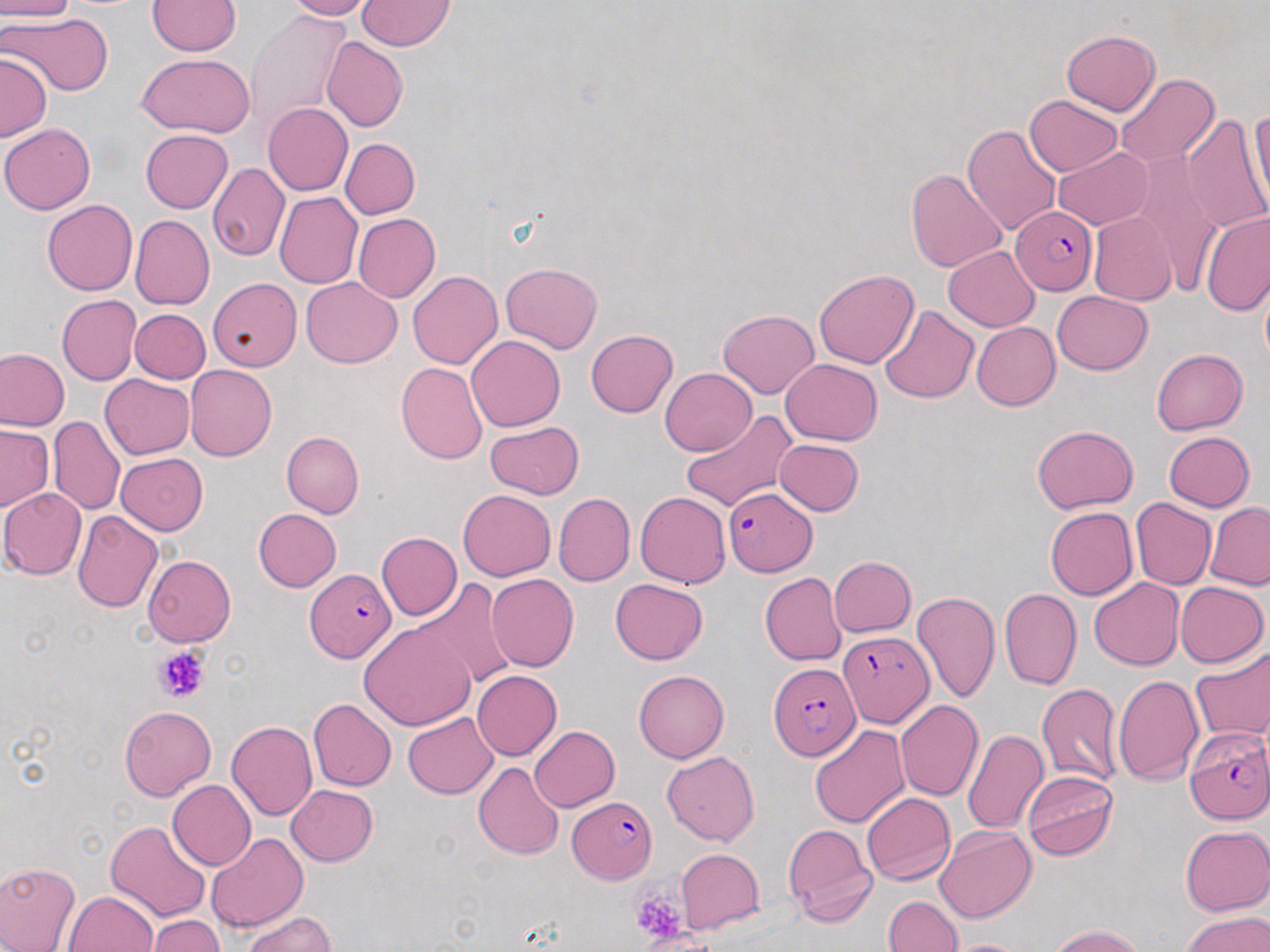

slide-level diagnosis = Plasmodium falciparum
modality = optical microscopy
preparation = thin blood smear
image size = 1270×952 pixels
magnification = 1000x
field of view = single
Plasmodium falciparum-infected red blood cell locations = approximate bounding boxes as (x1, y1, x2, y2) in pixels: (1014, 205, 1097, 292), (723, 486, 816, 576), (305, 567, 397, 663), (837, 632, 930, 728), (768, 661, 859, 761), (1185, 727, 1270, 826), (566, 796, 657, 883)
uninfected red blood cell locations = approximate bounding boxes as (x1, y1, x2, y2) in pixels: (0, 0, 76, 21), (281, 0, 373, 21), (356, 0, 454, 50), (147, 1, 242, 56), (246, 10, 353, 131), (3, 13, 112, 96), (1060, 30, 1160, 116), (322, 36, 408, 132), (0, 52, 51, 141), (137, 52, 254, 137), (1114, 74, 1221, 168), (1025, 94, 1122, 177), (263, 102, 352, 196), (1245, 109, 1270, 221), (1180, 114, 1268, 235), (0, 123, 95, 214), (962, 123, 1061, 238), (140, 129, 234, 213), (340, 139, 419, 219), (1054, 146, 1152, 229), (1130, 155, 1225, 295), (207, 162, 290, 262), (904, 167, 1008, 275), (274, 192, 362, 289), (42, 200, 137, 295), (1088, 211, 1176, 306), (1201, 211, 1270, 317), (353, 213, 440, 303), (129, 215, 214, 310), (943, 246, 1041, 332), (500, 262, 602, 354), (813, 269, 919, 369), (407, 271, 503, 370), (300, 277, 403, 368), (208, 278, 302, 372), (1052, 290, 1151, 374), (56, 295, 142, 385), (878, 305, 980, 404), (718, 308, 819, 399), (130, 309, 210, 383), (971, 322, 1060, 410), (585, 330, 677, 418), (467, 335, 565, 432), (0, 348, 70, 432), (1152, 349, 1248, 435), (782, 358, 882, 445), (396, 362, 488, 465), (185, 365, 277, 462), (660, 368, 757, 456), (100, 373, 194, 460), (680, 409, 796, 512), (48, 416, 125, 515), (485, 421, 584, 499), (0, 424, 53, 511), (1032, 425, 1138, 512), (281, 430, 364, 517), (1163, 431, 1255, 511), (774, 439, 864, 515), (116, 452, 208, 535), (1, 488, 87, 580), (457, 489, 555, 581), (635, 491, 730, 588), (553, 493, 635, 586), (1130, 497, 1216, 590), (1205, 501, 1270, 590), (1045, 507, 1138, 600), (253, 509, 341, 591), (72, 510, 163, 612), (376, 531, 462, 621), (142, 555, 235, 646), (828, 556, 917, 638), (759, 572, 845, 665), (487, 574, 579, 672), (611, 578, 708, 664), (1089, 578, 1185, 670), (415, 580, 518, 690), (1173, 581, 1268, 668), (1000, 589, 1082, 691), (912, 590, 1001, 703), (359, 619, 479, 730), (1190, 648, 1270, 744), (472, 670, 561, 761), (633, 670, 729, 763), (1113, 674, 1203, 785), (1036, 683, 1123, 786), (840, 698, 961, 812), (307, 699, 396, 791), (896, 700, 984, 801), (119, 704, 215, 800), (402, 713, 497, 798), (227, 721, 318, 820), (529, 725, 620, 812), (809, 725, 910, 827), (962, 729, 1048, 835), (662, 750, 759, 846), (473, 762, 564, 861), (1022, 771, 1117, 860), (167, 779, 256, 870), (286, 784, 379, 865), (861, 792, 955, 885), (106, 820, 211, 922), (782, 824, 876, 927), (935, 826, 1036, 923), (1180, 826, 1270, 915), (204, 831, 309, 934), (676, 849, 763, 934), (0, 860, 81, 952), (65, 891, 159, 952), (883, 895, 962, 951), (1182, 910, 1270, 951), (242, 912, 336, 952), (148, 915, 225, 952), (1049, 925, 1146, 952), (943, 939, 1033, 952)
stain = May-Grünwald-Giemsa
platelet locations = approximate bounding boxes as (x1, y1, x2, y2) in pixels: (154, 646, 210, 703), (630, 890, 697, 944)